Assess for malaria.
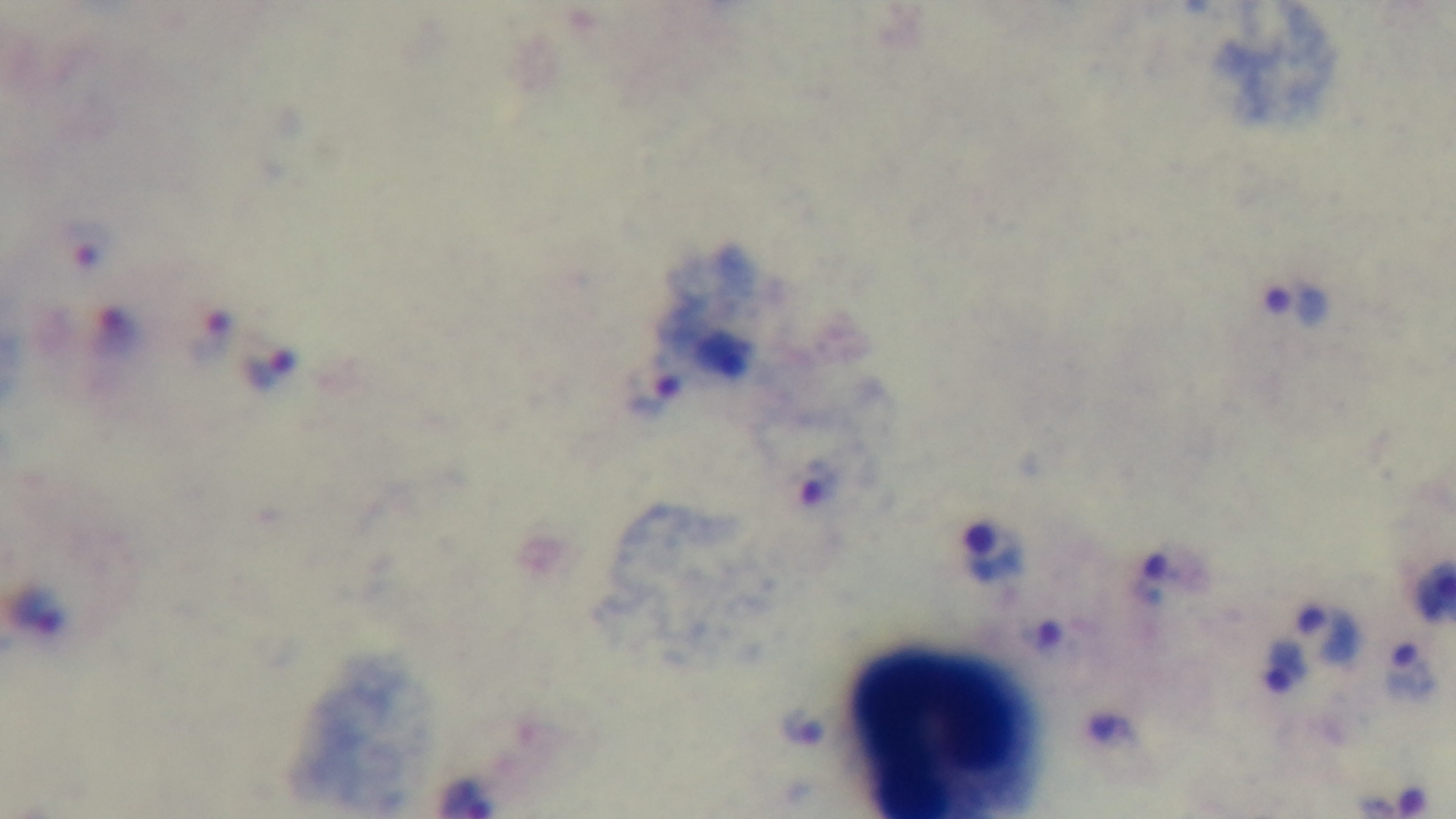

Infected.

Summary:
  - Field of view: one from the slide
  - Stain: Giemsa
  - Preparation: thick
  - Modality: light microscopy
  - Capture: mounted 4K digital camera
  - Objective: 100x oil immersion